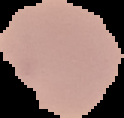 Result: no Plasmodium parasites seen. From a thin blood smear. The area outside the segmented cell region is set to black. Image is 124×118 pixels.